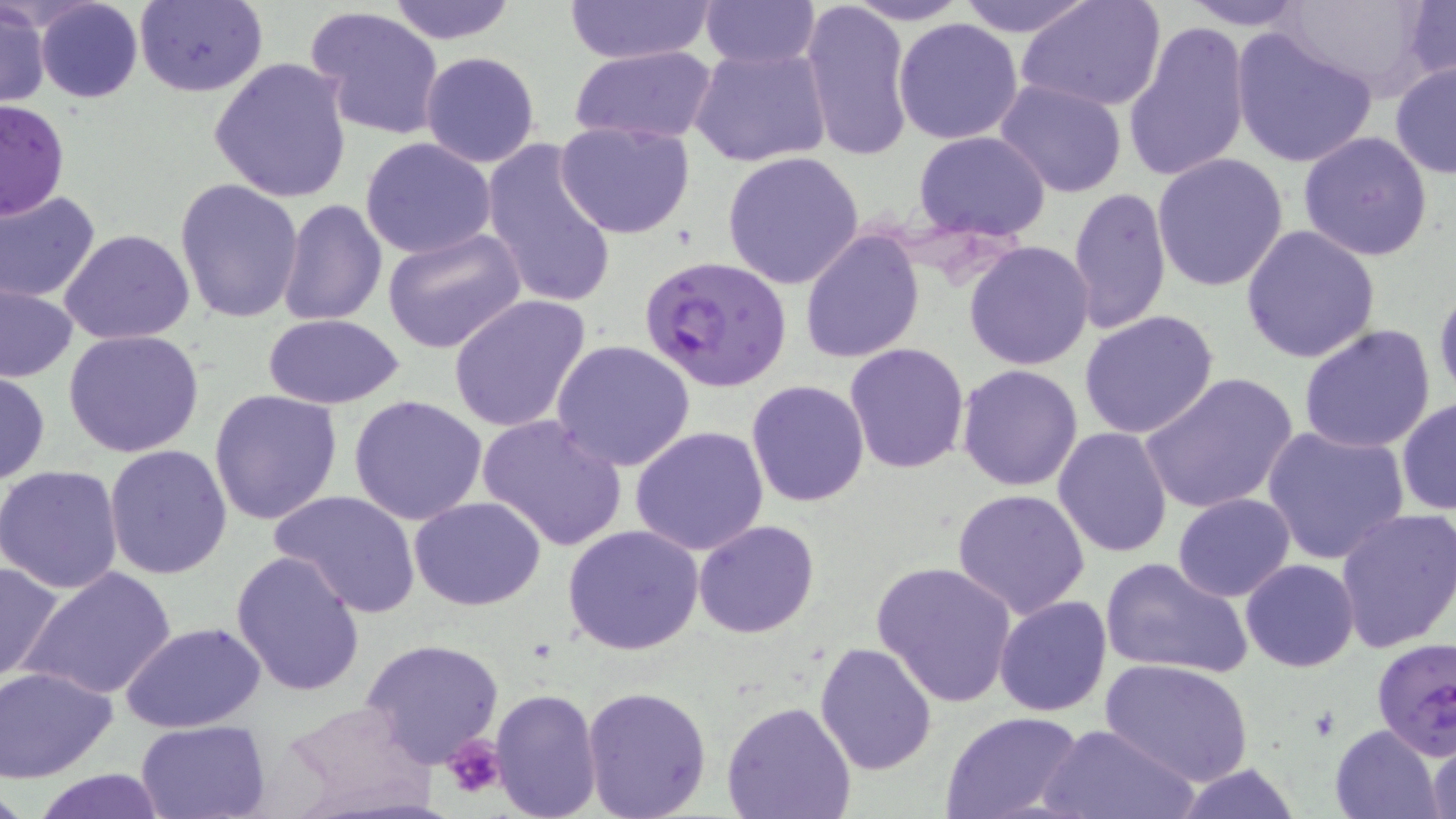

{
  "plasmodium_falciparum_infected_red_blood_cell_locations": "approximate bounding boxes as (x1, y1, x2, y2) in pixels: (641, 255, 792, 393), (1371, 637, 1456, 759)",
  "slide_level_diagnosis": "Plasmodium falciparum",
  "stain": "May-Grünwald-Giemsa",
  "platelet_locations": "approximate bounding boxes as (x1, y1, x2, y2) in pixels: (441, 732, 503, 800)",
  "image_size": "1456×819 pixels",
  "uninfected_red_blood_cell_locations": "approximate bounding boxes as (x1, y1, x2, y2) in pixels: (385, 0, 517, 44), (562, 0, 714, 64), (698, 0, 819, 69), (957, 0, 1097, 37), (1015, 0, 1167, 114), (1178, 0, 1312, 30), (1281, 0, 1439, 100), (35, 1, 142, 103), (133, 1, 268, 97), (800, 1, 913, 163), (843, 1, 972, 25), (1402, 1, 1455, 86), (0, 2, 49, 108), (306, 5, 446, 141), (893, 18, 1024, 145), (1123, 21, 1250, 184), (1231, 29, 1379, 170), (569, 44, 717, 145), (690, 44, 832, 169), (419, 51, 540, 168), (209, 57, 352, 203), (1389, 60, 1456, 180), (993, 79, 1128, 200), (0, 98, 69, 219), (553, 119, 697, 240), (913, 130, 1053, 242), (1298, 130, 1433, 261), (480, 136, 618, 312), (361, 137, 496, 260), (721, 151, 865, 290), (1152, 153, 1291, 291), (176, 178, 306, 324), (1068, 187, 1171, 336), (0, 189, 101, 302), (278, 198, 388, 326), (1241, 225, 1383, 363), (382, 227, 528, 355), (60, 229, 196, 346), (800, 229, 924, 363), (964, 241, 1095, 371), (1434, 281, 1456, 403), (1, 286, 78, 381), (448, 294, 591, 434), (1079, 310, 1219, 438), (263, 313, 405, 409), (1298, 323, 1437, 454), (62, 331, 206, 459), (551, 338, 696, 471), (844, 342, 969, 474), (956, 364, 1084, 491), (0, 370, 50, 486), (1138, 372, 1298, 516), (746, 379, 871, 506), (210, 388, 343, 524), (348, 394, 487, 525), (1397, 397, 1455, 516), (478, 413, 628, 554), (628, 424, 771, 556), (1053, 426, 1176, 558), (1261, 426, 1408, 564), (105, 444, 234, 581), (1, 464, 124, 593), (952, 488, 1090, 618), (270, 490, 421, 617), (1172, 493, 1294, 602), (410, 495, 547, 609), (1334, 508, 1456, 656), (974, 509, 1105, 705), (696, 520, 820, 638), (562, 525, 704, 655), (228, 548, 367, 697), (1101, 555, 1253, 678), (0, 558, 63, 683), (1241, 559, 1359, 671), (870, 560, 1019, 708), (21, 565, 178, 703), (993, 595, 1111, 717), (120, 621, 265, 733), (357, 638, 506, 769), (814, 640, 939, 774), (1101, 659, 1252, 788), (0, 665, 120, 784), (582, 683, 712, 819), (488, 687, 604, 819), (720, 700, 858, 819), (277, 702, 438, 817), (940, 711, 1083, 819), (135, 719, 272, 819), (1040, 721, 1196, 819), (1329, 722, 1445, 819), (1427, 734, 1455, 819), (1168, 764, 1307, 819), (27, 767, 170, 819)",
  "modality": "optical microscopy",
  "magnification": "1000x",
  "preparation": "thin blood film",
  "field_of_view": "one of a larger specimen"
}